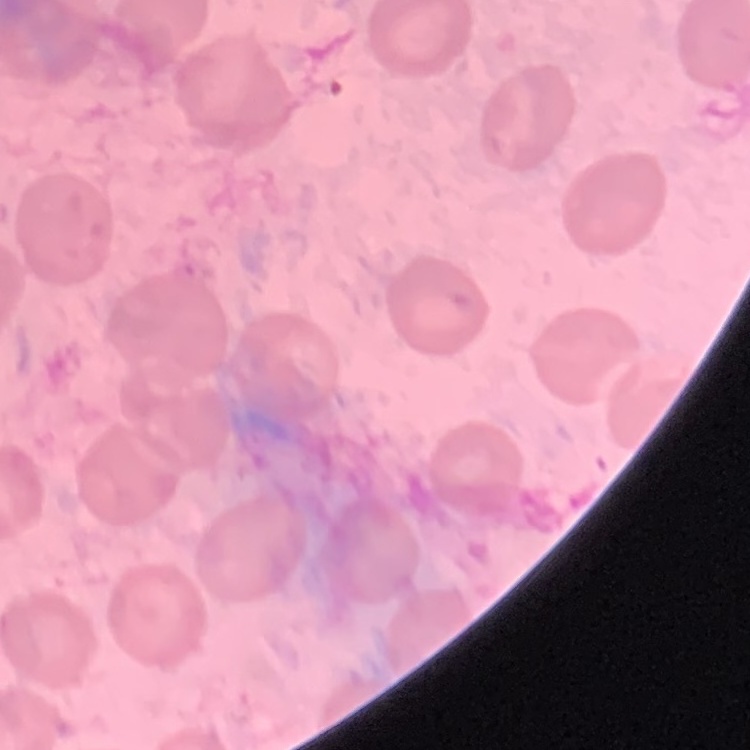
Summary:
  - Erythrocyte morphology: no rouleaux formation
  - Stain: Field's or Giemsa
  - Preparation: thin peripheral smear
  - Image type: square crop of a larger photomicrograph